Classify this cell by malaria status.
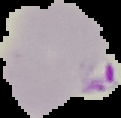

Parasitized.

{
  "image_type": "segmented cell region on a black background",
  "image_size": "121×118 pixels",
  "preparation": "thin blood film"
}